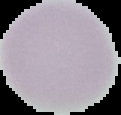
result: negative for malaria parasites
preparation: thin blood film
image_size: 121×115 pixels
image_type: segmented cell region with the area outside set to black